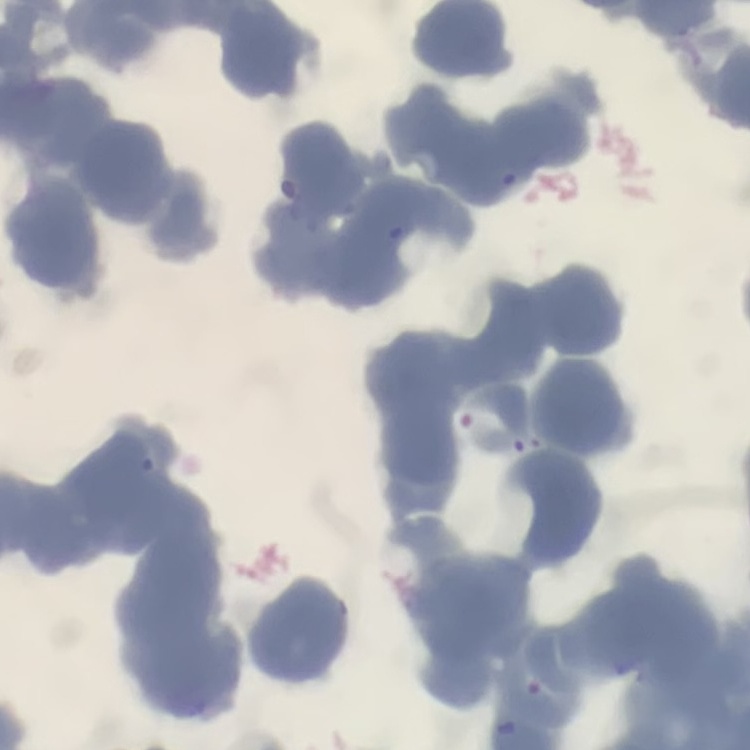
red_blood_cell_morphology: rouleaux formation
image_type: one tile cut from a larger photomicrograph
preparation: thin blood smear
stain: Field's or Giemsa